Assess this cell for malaria.
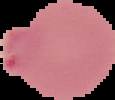
It is parasitized.

preparation = thin blood film
image type = segmented cell region with the area outside set to black
image size = 115×100 pixels